Give the extent of all Plasmodium falciparum-infected red blood cells.
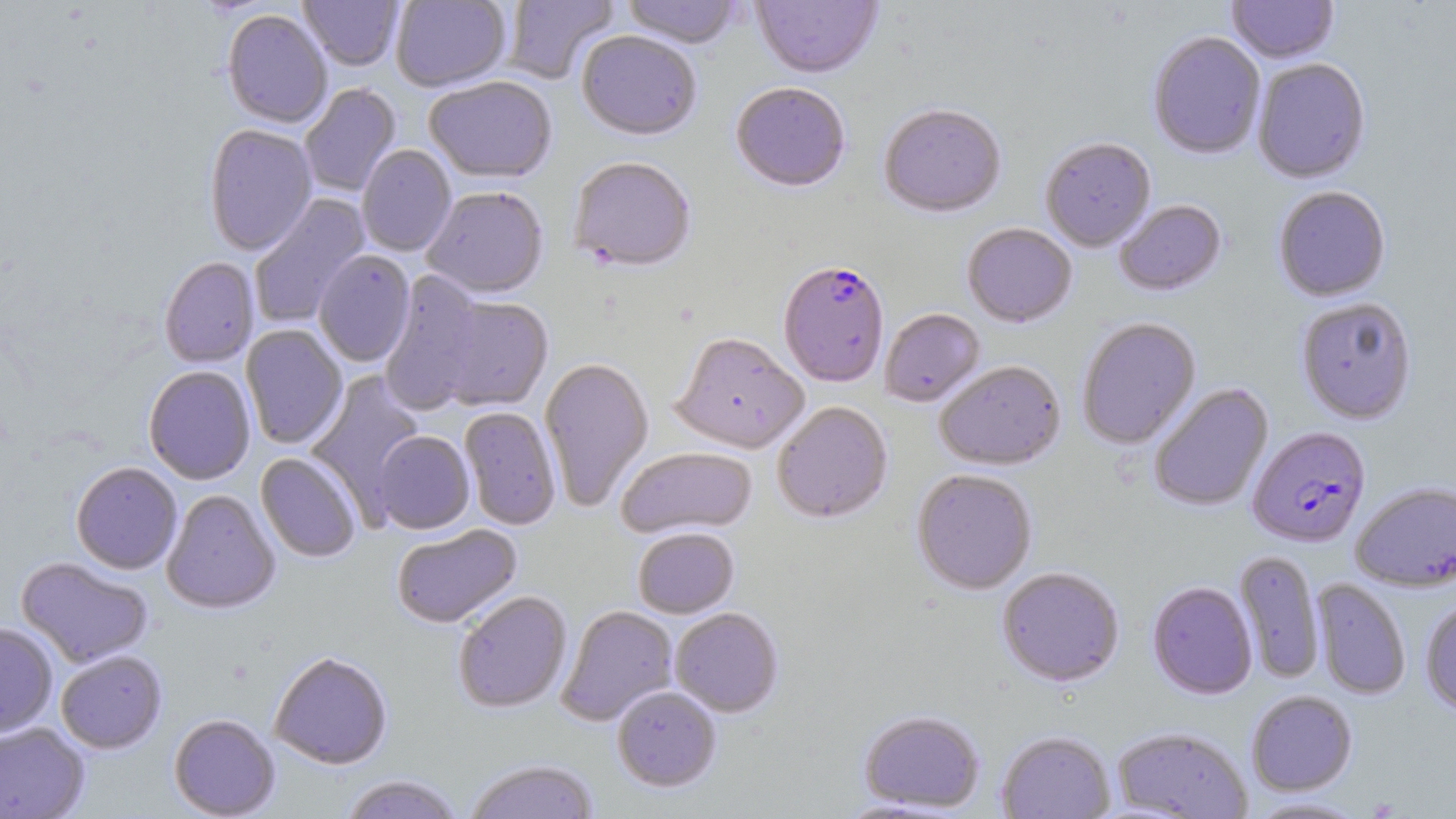
Approximate bounding boxes as named x1/y1/x2/y2 corners in pixels.
Plasmodium falciparum-infected red blood cells: (x1=778, y1=264, x2=889, y2=389), (x1=1247, y1=427, x2=1370, y2=548).

Summary:
  - Uninfected red blood cell locations: (x1=298, y1=0, x2=404, y2=72), (x1=391, y1=0, x2=512, y2=93), (x1=503, y1=0, x2=619, y2=85), (x1=620, y1=0, x2=743, y2=51), (x1=751, y1=0, x2=883, y2=82), (x1=1227, y1=0, x2=1339, y2=65), (x1=222, y1=10, x2=332, y2=130), (x1=577, y1=32, x2=701, y2=143), (x1=1148, y1=32, x2=1266, y2=161), (x1=1253, y1=60, x2=1370, y2=185), (x1=424, y1=78, x2=557, y2=186), (x1=300, y1=84, x2=402, y2=198), (x1=730, y1=84, x2=850, y2=195), (x1=878, y1=106, x2=1006, y2=219), (x1=204, y1=125, x2=317, y2=256), (x1=1040, y1=139, x2=1156, y2=252), (x1=357, y1=145, x2=456, y2=257), (x1=568, y1=160, x2=696, y2=275), (x1=1273, y1=187, x2=1391, y2=302), (x1=422, y1=188, x2=549, y2=301), (x1=248, y1=194, x2=370, y2=329), (x1=1114, y1=200, x2=1227, y2=297), (x1=962, y1=224, x2=1076, y2=328), (x1=314, y1=251, x2=415, y2=367), (x1=159, y1=257, x2=260, y2=368), (x1=379, y1=271, x2=489, y2=415), (x1=434, y1=295, x2=554, y2=412), (x1=1296, y1=298, x2=1417, y2=425), (x1=880, y1=309, x2=985, y2=408), (x1=1077, y1=318, x2=1201, y2=450), (x1=240, y1=324, x2=348, y2=450), (x1=670, y1=334, x2=809, y2=454), (x1=539, y1=358, x2=654, y2=512), (x1=935, y1=361, x2=1065, y2=471), (x1=143, y1=366, x2=256, y2=485), (x1=305, y1=370, x2=427, y2=514), (x1=1149, y1=383, x2=1273, y2=512), (x1=772, y1=403, x2=893, y2=525), (x1=459, y1=407, x2=561, y2=531), (x1=373, y1=431, x2=474, y2=535), (x1=616, y1=448, x2=757, y2=540), (x1=256, y1=453, x2=362, y2=563), (x1=70, y1=462, x2=182, y2=575), (x1=912, y1=470, x2=1037, y2=596), (x1=1351, y1=482, x2=1456, y2=592), (x1=161, y1=489, x2=280, y2=614), (x1=391, y1=525, x2=523, y2=630), (x1=633, y1=529, x2=739, y2=619), (x1=1234, y1=550, x2=1324, y2=683), (x1=16, y1=557, x2=154, y2=668), (x1=997, y1=567, x2=1124, y2=688), (x1=1311, y1=578, x2=1411, y2=700), (x1=1147, y1=581, x2=1257, y2=700), (x1=453, y1=591, x2=572, y2=714), (x1=1420, y1=599, x2=1456, y2=715), (x1=556, y1=605, x2=678, y2=726), (x1=670, y1=608, x2=783, y2=718), (x1=0, y1=622, x2=58, y2=737), (x1=56, y1=650, x2=167, y2=754), (x1=269, y1=651, x2=393, y2=770), (x1=612, y1=687, x2=721, y2=793), (x1=1246, y1=690, x2=1357, y2=796), (x1=859, y1=710, x2=985, y2=813), (x1=169, y1=714, x2=280, y2=818), (x1=0, y1=723, x2=90, y2=819), (x1=1111, y1=726, x2=1252, y2=818), (x1=997, y1=731, x2=1114, y2=818), (x1=462, y1=759, x2=599, y2=819), (x1=338, y1=775, x2=466, y2=819), (x1=1246, y1=796, x2=1370, y2=818)
  - Slide-level diagnosis: Plasmodium falciparum
  - Modality: light microscopy
  - Field of view: one of a larger specimen
  - Preparation: thin blood film
  - Stain: May-Grünwald-Giemsa
  - Magnification: 1000x
  - Image size: 1456×819 pixels